Point out each malaria parasite.
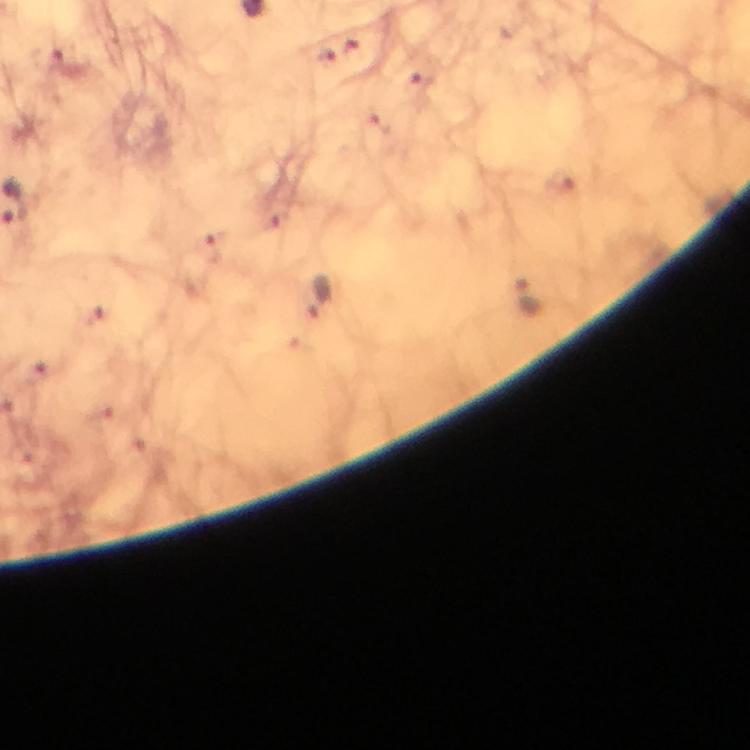
Approximate centers as {x, y} in pixels.
Malaria parasites: {530, 297}, {319, 298}.

From a diagnostic examination for malaria. 100x magnification. Image is 750×750 pixels. Cropped region of a single field of view. Immersion oil was used. Photographed through the microscope with a smartphone camera. Giemsa-stained preparation. Thick blood film.